Classify the preparation.
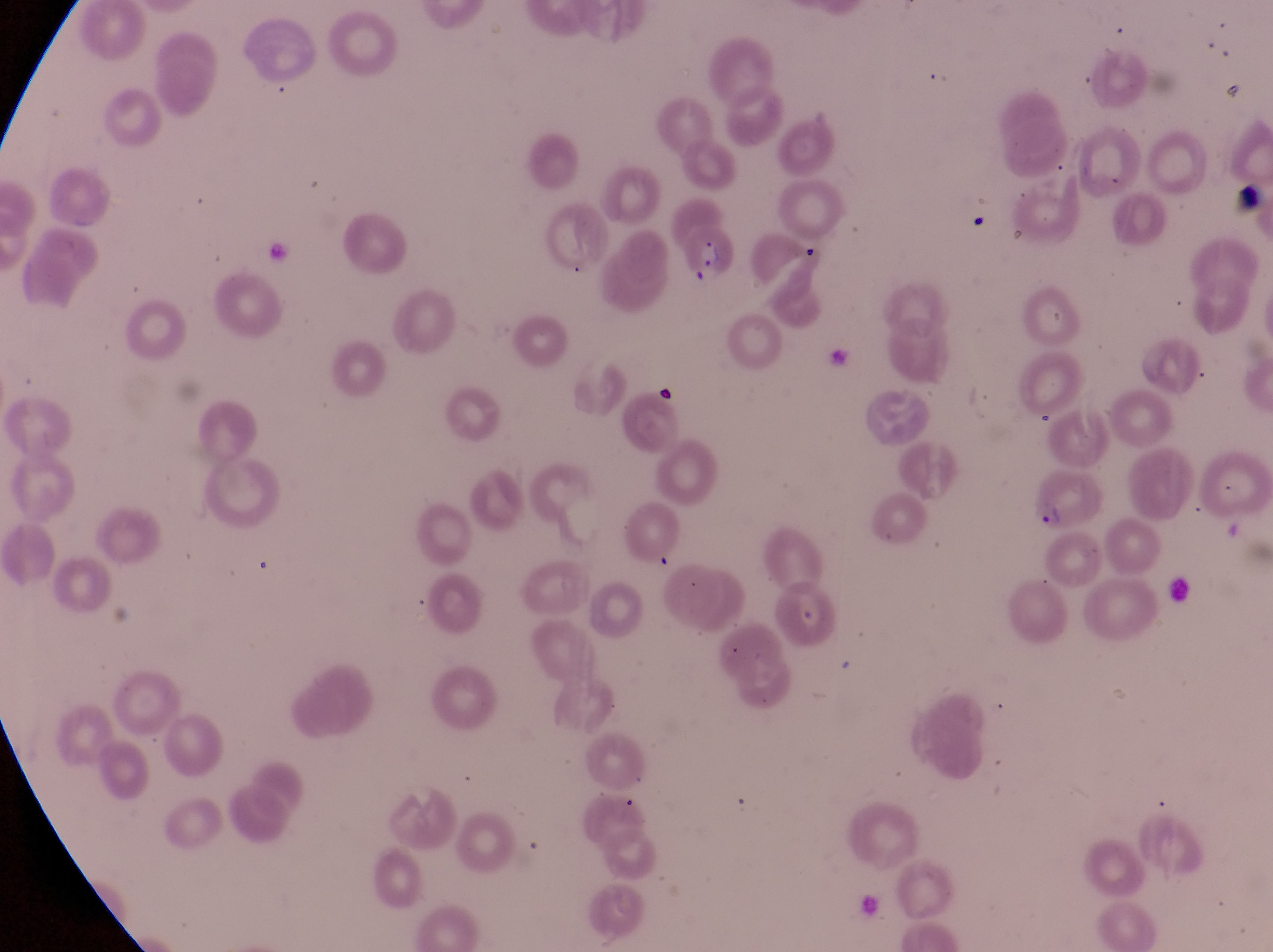

This is a thin smear.

Approximate bounding boxes as {left, top, right, bottom} in pixels.
Summary:
  - Artifact (platelet-like body, stain precipitate, or debris) locations: {1231, 175, 1271, 227}, {644, 359, 679, 409}
  - Parasitised red blood cell locations: {676, 217, 741, 292}, {1026, 465, 1113, 530}
  - Country: Uganda
  - Magnification: 1000x
  - Capture: smartphone photograph through the eyepiece of an Olympus CX-23 microscope
  - Image size: 1273×952 pixels
  - Field of view: single